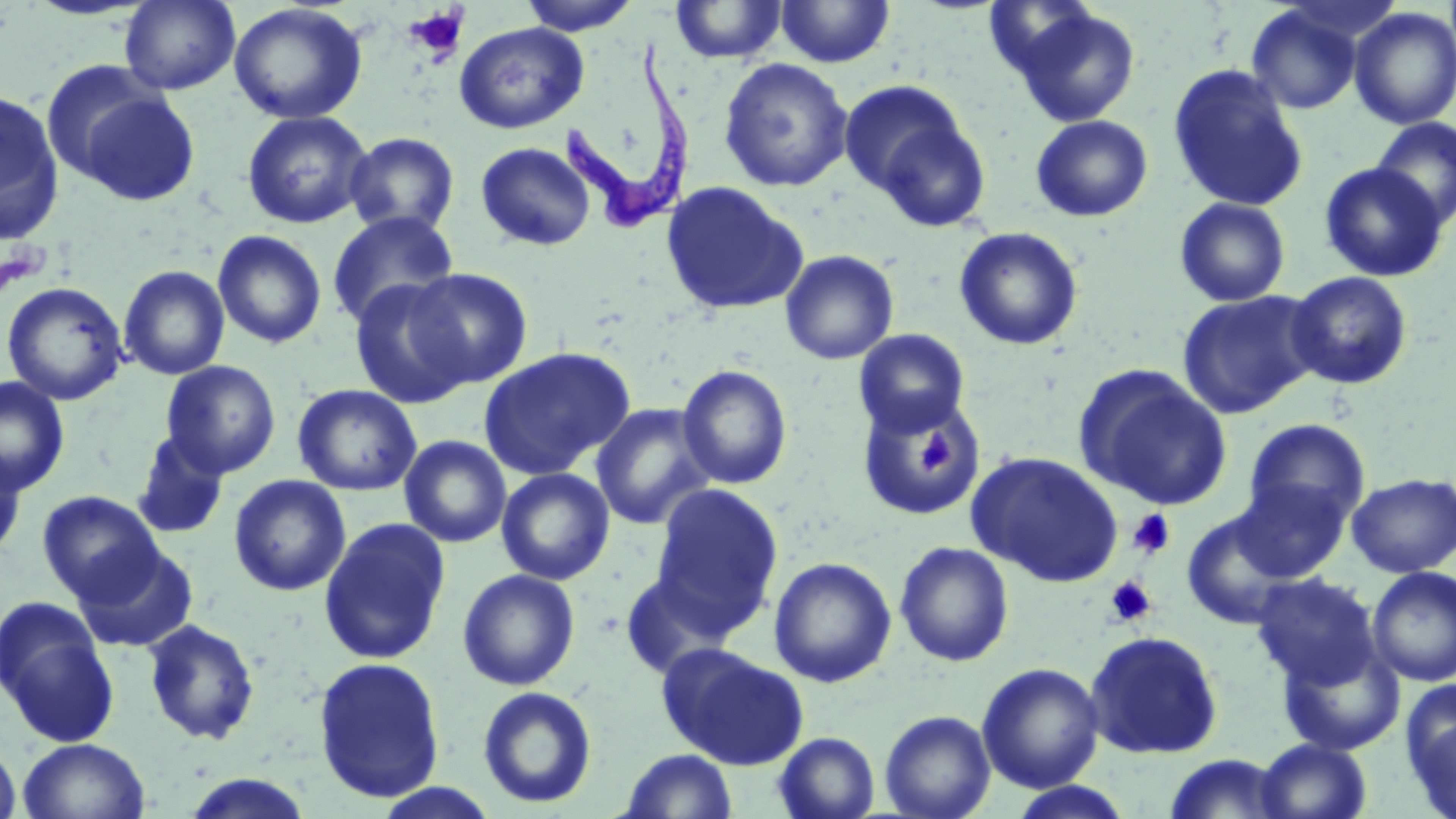
Summary:
  - Coordinate format: approximate bounding boxes as [x1, y1, x2, y2] in pixels
  - Uninfected red blood cell locations: [517, 0, 643, 35], [776, 0, 895, 68], [119, 1, 240, 94], [669, 1, 787, 64], [228, 3, 368, 124], [1008, 5, 1142, 127], [1246, 5, 1363, 115], [1349, 7, 1456, 130], [454, 22, 589, 134], [718, 57, 854, 192], [39, 60, 168, 189], [1167, 64, 1309, 212], [840, 80, 972, 206], [74, 87, 201, 208], [0, 88, 65, 244], [241, 110, 373, 229], [869, 113, 993, 232], [1030, 115, 1153, 222], [1370, 117, 1456, 230], [343, 131, 460, 237], [475, 141, 596, 251], [1319, 162, 1448, 282], [660, 181, 808, 316], [1174, 197, 1290, 307], [326, 211, 459, 329], [212, 224, 454, 340], [954, 226, 1083, 351], [212, 230, 327, 349], [779, 250, 899, 365], [118, 264, 230, 380], [406, 268, 533, 388], [1287, 271, 1413, 390], [349, 278, 475, 409], [1, 281, 129, 405], [1177, 290, 1322, 419], [854, 329, 970, 436], [478, 346, 635, 480], [160, 360, 281, 478], [677, 364, 793, 489], [1075, 366, 1232, 510], [0, 375, 70, 497], [293, 384, 422, 496], [856, 395, 988, 521], [590, 404, 716, 530], [1243, 418, 1370, 527], [131, 431, 230, 540], [399, 435, 512, 548], [0, 445, 27, 562], [967, 451, 1124, 587], [496, 467, 614, 585], [1346, 473, 1456, 577], [229, 474, 351, 596], [1231, 477, 1352, 582], [649, 484, 783, 631], [37, 490, 163, 604], [1181, 508, 1304, 630], [318, 517, 451, 665], [894, 541, 1014, 667], [73, 544, 197, 652], [768, 557, 897, 688], [1367, 566, 1456, 687], [457, 569, 580, 690], [619, 569, 736, 678], [1252, 573, 1381, 690], [0, 598, 119, 748], [143, 619, 260, 746], [1084, 629, 1224, 760], [1277, 640, 1405, 756], [658, 644, 808, 770], [312, 655, 446, 803], [976, 662, 1105, 793], [477, 686, 597, 809], [1404, 689, 1456, 818], [879, 709, 996, 819], [774, 731, 880, 819], [0, 738, 23, 819], [16, 738, 151, 819], [1255, 738, 1372, 819], [620, 749, 738, 818], [1162, 753, 1292, 818], [180, 772, 315, 818], [1005, 782, 1137, 818], [370, 783, 502, 819]
  - Platelet locations: [404, 5, 469, 62], [912, 430, 959, 479], [1128, 509, 1175, 558], [1105, 576, 1156, 626]
  - Trypanosoma brucei locations: [562, 37, 695, 237]
  - Slide-level diagnosis: Trypanosoma brucei
  - Field of view: single
  - Magnification: 1000x
  - Modality: light microscopy
  - Preparation: thin blood film
  - Stain: May-Grünwald-Giemsa
  - Image size: 1456×819 pixels